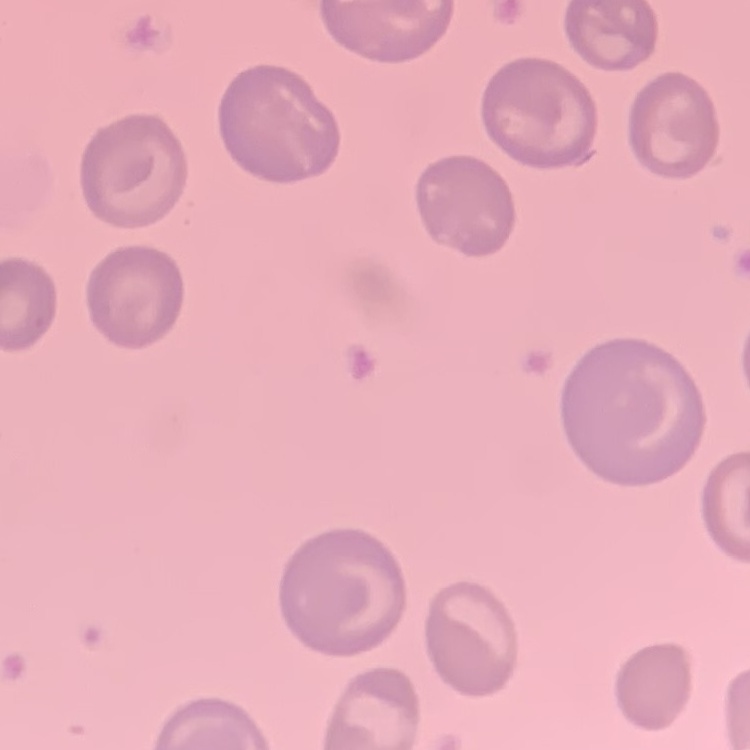 The red blood cells exhibit no rouleaux formation. One tile cut from a larger photomicrograph. Thin blood smear. Field's or Giemsa stain.